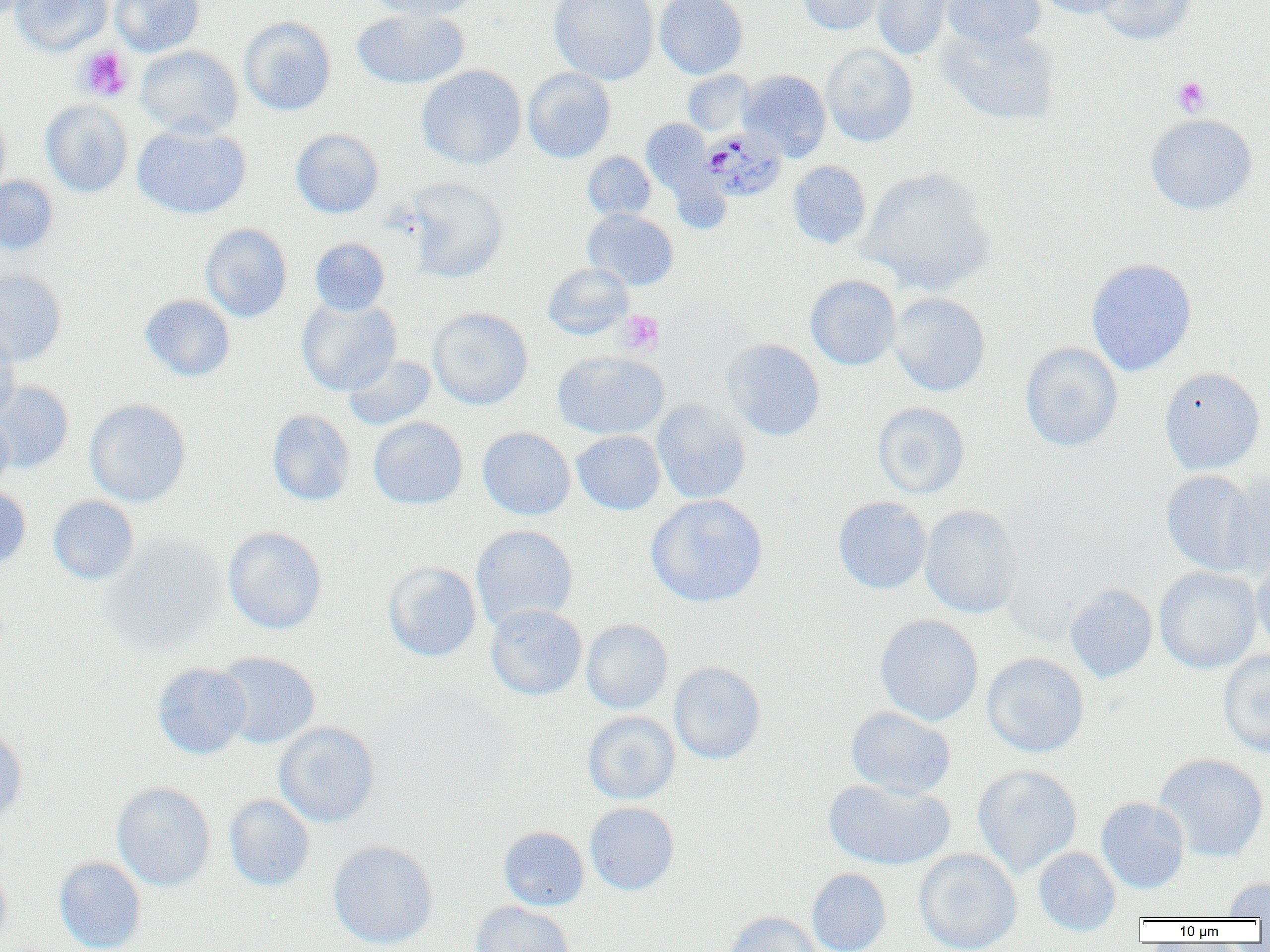
Approximate bounding boxes as (x1, y1, x2, y2) in pixels. Uninfected red blood cell locations: (0, 0, 41, 20), (10, 0, 112, 56), (110, 0, 205, 57), (365, 0, 479, 20), (548, 0, 659, 85), (654, 0, 748, 79), (795, 0, 887, 35), (871, 0, 961, 61), (942, 0, 1045, 50), (1032, 0, 1129, 18), (1093, 0, 1196, 45), (352, 8, 469, 90), (239, 17, 336, 116), (937, 24, 1060, 126), (821, 44, 918, 146), (136, 45, 244, 139), (416, 65, 527, 170), (523, 68, 616, 163), (683, 70, 756, 136), (737, 70, 831, 161), (40, 100, 133, 197), (0, 107, 10, 201), (1145, 114, 1258, 216), (641, 119, 714, 197), (132, 124, 251, 219), (290, 129, 384, 218), (582, 151, 656, 221), (787, 160, 872, 249), (860, 167, 995, 295), (0, 176, 59, 256), (404, 178, 508, 283), (583, 209, 679, 290), (200, 223, 292, 322), (310, 238, 390, 316), (1086, 257, 1197, 376), (542, 262, 633, 339), (0, 268, 67, 366), (805, 275, 901, 370), (888, 292, 991, 397), (139, 294, 235, 381), (296, 297, 401, 395), (427, 307, 533, 409), (0, 332, 19, 423), (722, 338, 825, 441), (1020, 342, 1123, 451), (552, 351, 669, 439), (344, 354, 436, 430), (1159, 367, 1266, 475), (0, 381, 74, 473), (651, 398, 751, 504), (84, 399, 191, 507), (872, 402, 970, 499), (267, 409, 355, 506), (0, 414, 15, 494), (368, 417, 468, 509), (477, 427, 575, 520), (572, 430, 665, 515), (1161, 469, 1263, 575), (1221, 469, 1270, 580), (0, 485, 31, 571), (645, 494, 768, 607), (48, 496, 139, 585), (833, 496, 932, 594), (919, 504, 1023, 619), (471, 525, 578, 629), (224, 526, 327, 634), (103, 533, 226, 653), (1251, 555, 1270, 656), (383, 561, 482, 662), (1153, 566, 1262, 674), (1065, 584, 1157, 683), (486, 604, 587, 700), (874, 614, 984, 725), (581, 619, 673, 714), (1218, 649, 1270, 756), (214, 652, 320, 749), (981, 652, 1089, 757), (669, 661, 766, 765), (153, 662, 252, 758), (845, 706, 956, 798), (582, 711, 680, 804), (274, 722, 380, 828), (0, 727, 28, 831), (1154, 753, 1269, 861), (972, 764, 1082, 878), (823, 778, 954, 871), (112, 782, 215, 891), (224, 794, 315, 891), (1096, 797, 1190, 893), (584, 802, 680, 895), (498, 826, 589, 910), (327, 840, 438, 949), (1033, 847, 1121, 936), (914, 849, 1022, 952), (54, 856, 147, 952), (0, 860, 12, 948), (807, 868, 891, 952), (1223, 876, 1270, 918), (471, 901, 575, 952), (723, 911, 821, 952). Platelet locations: (76, 46, 133, 102), (1172, 76, 1211, 117), (618, 310, 665, 356). Plasmodium malariae-infected red blood cell locations: (700, 128, 787, 202). Slide-level diagnosis: Plasmodium malariae. Captured at 1000x magnification. Thin blood film. Light microscopy. Image is 1270×952 pixels. Single field of view.